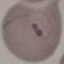
Summary:
  - Result: malaria parasites detected
  - Capture: smartphone through the microscope eyepiece
  - Image type: automatically extracted cell patch, resized to 64 × 64 pixels
  - Stain: Giemsa
  - Preparation: thin blood film